Give the position of every Plasmodium parasite visible.
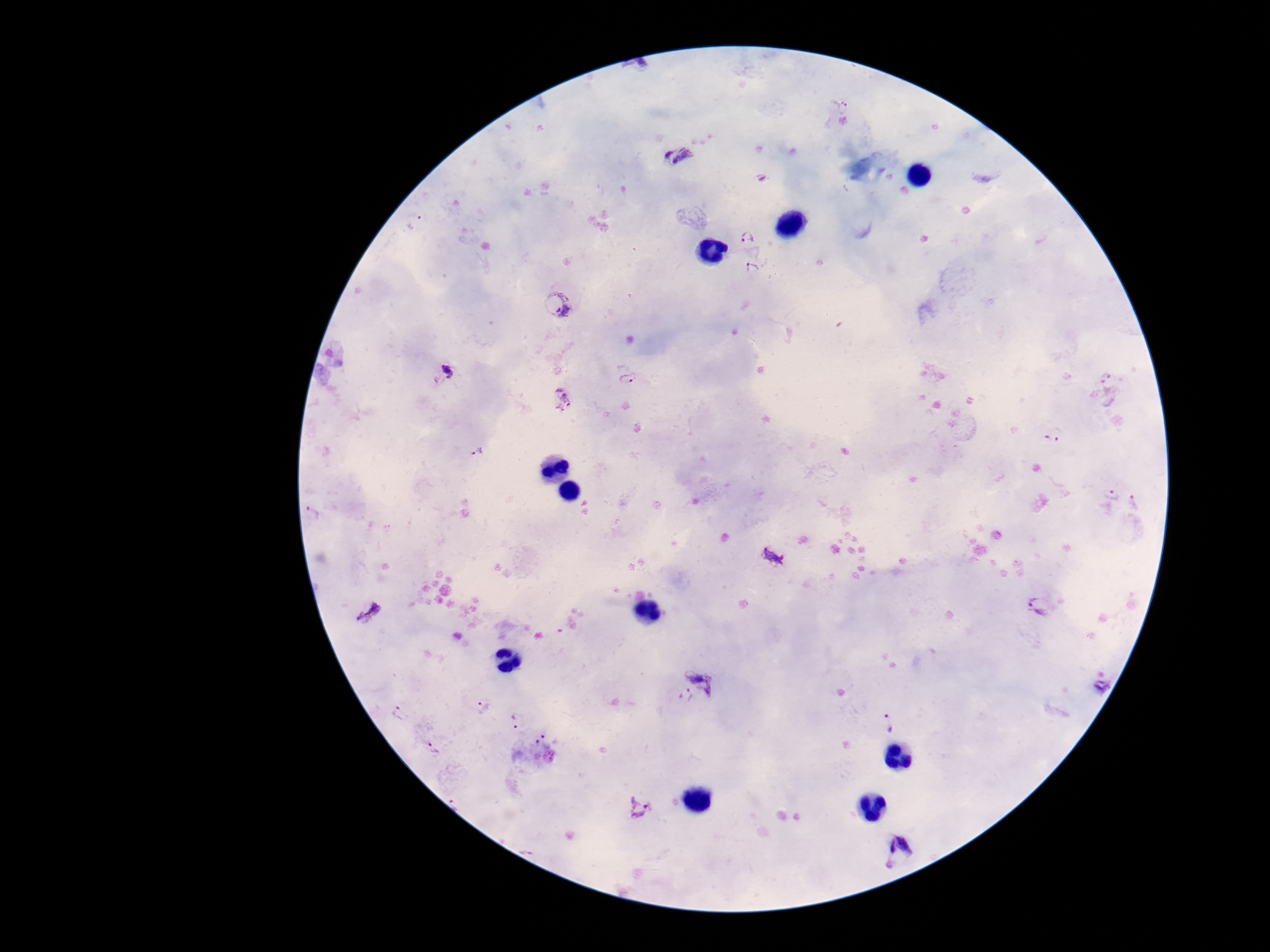

Approximate object centers, in pixels from the top-left corner.
Plasmodium parasites: (x=843, y=107), (x=679, y=155), (x=416, y=223), (x=747, y=237), (x=752, y=270), (x=558, y=304), (x=440, y=374), (x=629, y=378), (x=561, y=398), (x=1054, y=434), (x=478, y=452), (x=1111, y=495), (x=312, y=514), (x=774, y=558), (x=1040, y=606), (x=369, y=610), (x=708, y=674), (x=1101, y=687), (x=686, y=694), (x=482, y=706), (x=402, y=713), (x=518, y=720), (x=891, y=722), (x=543, y=741), (x=435, y=751), (x=640, y=808), (x=900, y=854).

stain = Giemsa
preparation = thick blood film
capture = smartphone camera through the microscope eyepiece
patient malaria status = infected
magnification = 100x
image size = 1270×952 pixels
field of view = single